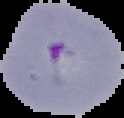

Cell region segmented out of the field of view; the surrounding area is masked to black. From a thin blood film. Image is 124×118 pixels. Malaria status: parasitized.